Name the parasite shown.
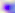
Toxoplasma gondii.

modality = micrograph
magnification = 400x